Describe the morphology of the erythrocytes.
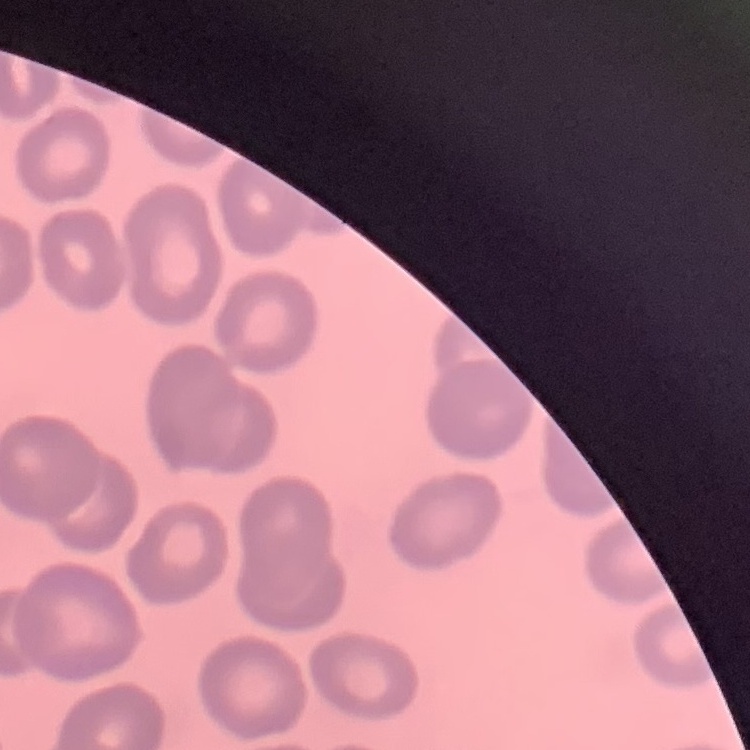

No rouleaux formation.

One tile cut from a larger photomicrograph. Thin peripheral smear. Field's or Giemsa stain.